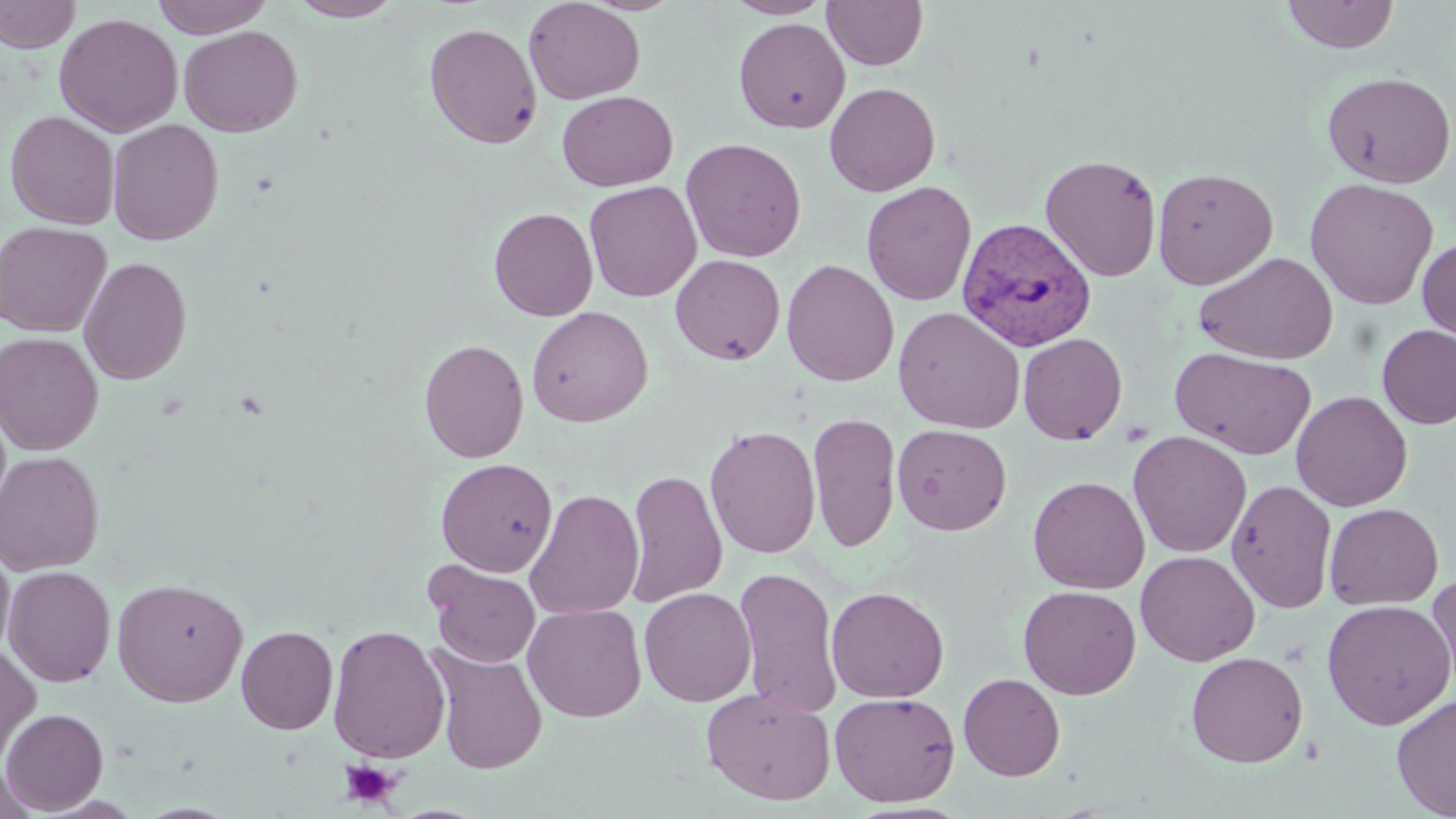

Summary:
  - Coordinate format: approximate bounding boxes as named x1/y1/x2/y2 corners in pixels
  - Platelet locations: (x1=339, y1=759, x2=401, y2=808)
  - Plasmodium vivax-infected red blood cell locations: (x1=957, y1=216, x2=1096, y2=351)
  - Uninfected red blood cell locations: (x1=0, y1=0, x2=80, y2=53), (x1=151, y1=0, x2=274, y2=38), (x1=288, y1=0, x2=404, y2=21), (x1=523, y1=0, x2=645, y2=105), (x1=725, y1=0, x2=833, y2=18), (x1=822, y1=0, x2=928, y2=70), (x1=1281, y1=0, x2=1400, y2=54), (x1=54, y1=13, x2=183, y2=137), (x1=733, y1=17, x2=850, y2=134), (x1=424, y1=22, x2=542, y2=149), (x1=179, y1=25, x2=302, y2=137), (x1=1321, y1=71, x2=1456, y2=189), (x1=824, y1=82, x2=941, y2=196), (x1=557, y1=90, x2=678, y2=192), (x1=4, y1=110, x2=120, y2=229), (x1=107, y1=118, x2=224, y2=245), (x1=681, y1=137, x2=807, y2=263), (x1=1040, y1=153, x2=1162, y2=282), (x1=1152, y1=167, x2=1278, y2=289), (x1=1304, y1=178, x2=1439, y2=310), (x1=584, y1=180, x2=702, y2=302), (x1=861, y1=181, x2=977, y2=306), (x1=1170, y1=183, x2=1311, y2=353), (x1=489, y1=206, x2=598, y2=321), (x1=0, y1=221, x2=112, y2=337), (x1=1417, y1=237, x2=1456, y2=345), (x1=1194, y1=251, x2=1339, y2=364), (x1=670, y1=254, x2=785, y2=365), (x1=78, y1=256, x2=192, y2=385), (x1=782, y1=259, x2=899, y2=387), (x1=527, y1=306, x2=653, y2=427), (x1=893, y1=306, x2=1025, y2=433), (x1=1376, y1=324, x2=1456, y2=429), (x1=0, y1=332, x2=104, y2=455), (x1=1018, y1=332, x2=1127, y2=445), (x1=419, y1=339, x2=529, y2=463), (x1=1170, y1=346, x2=1317, y2=460), (x1=1291, y1=390, x2=1413, y2=512), (x1=807, y1=411, x2=902, y2=552), (x1=705, y1=424, x2=821, y2=559), (x1=892, y1=424, x2=1012, y2=536), (x1=1128, y1=430, x2=1252, y2=558), (x1=0, y1=450, x2=104, y2=575), (x1=435, y1=458, x2=558, y2=577), (x1=624, y1=468, x2=728, y2=609), (x1=1027, y1=476, x2=1150, y2=594), (x1=1226, y1=478, x2=1337, y2=613), (x1=525, y1=487, x2=644, y2=619), (x1=1324, y1=503, x2=1444, y2=610), (x1=0, y1=545, x2=15, y2=662), (x1=1136, y1=550, x2=1260, y2=666), (x1=426, y1=561, x2=541, y2=667), (x1=3, y1=565, x2=116, y2=687), (x1=734, y1=565, x2=843, y2=717), (x1=1427, y1=571, x2=1456, y2=697), (x1=112, y1=577, x2=249, y2=706), (x1=1018, y1=584, x2=1141, y2=699), (x1=827, y1=586, x2=950, y2=704), (x1=639, y1=587, x2=757, y2=706), (x1=1321, y1=598, x2=1455, y2=730), (x1=523, y1=603, x2=646, y2=722), (x1=327, y1=624, x2=450, y2=764), (x1=236, y1=625, x2=338, y2=734), (x1=0, y1=642, x2=41, y2=768), (x1=427, y1=644, x2=548, y2=774), (x1=1186, y1=651, x2=1308, y2=767), (x1=958, y1=672, x2=1066, y2=781), (x1=701, y1=687, x2=836, y2=805), (x1=829, y1=691, x2=960, y2=807), (x1=1391, y1=693, x2=1456, y2=818), (x1=1, y1=708, x2=108, y2=814), (x1=0, y1=763, x2=39, y2=819)
  - Slide-level diagnosis: Plasmodium vivax
  - Modality: light microscopy
  - Stain: May-Grünwald-Giemsa
  - Image size: 1456×819 pixels
  - Magnification: 1000x
  - Field of view: one of a larger specimen
  - Preparation: thin blood smear